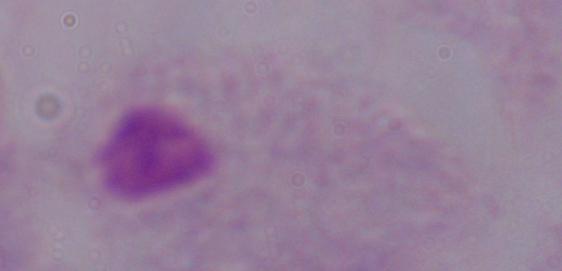

magnification = 1000x
identification = trichomonad
modality = micrograph